Classify this cell by malaria status.
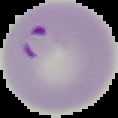

Parasitized.

Summary:
  - Image size: 118×118 pixels
  - Image type: cell region segmented out of the field of view; surrounding area masked to black
  - Preparation: thin blood smear